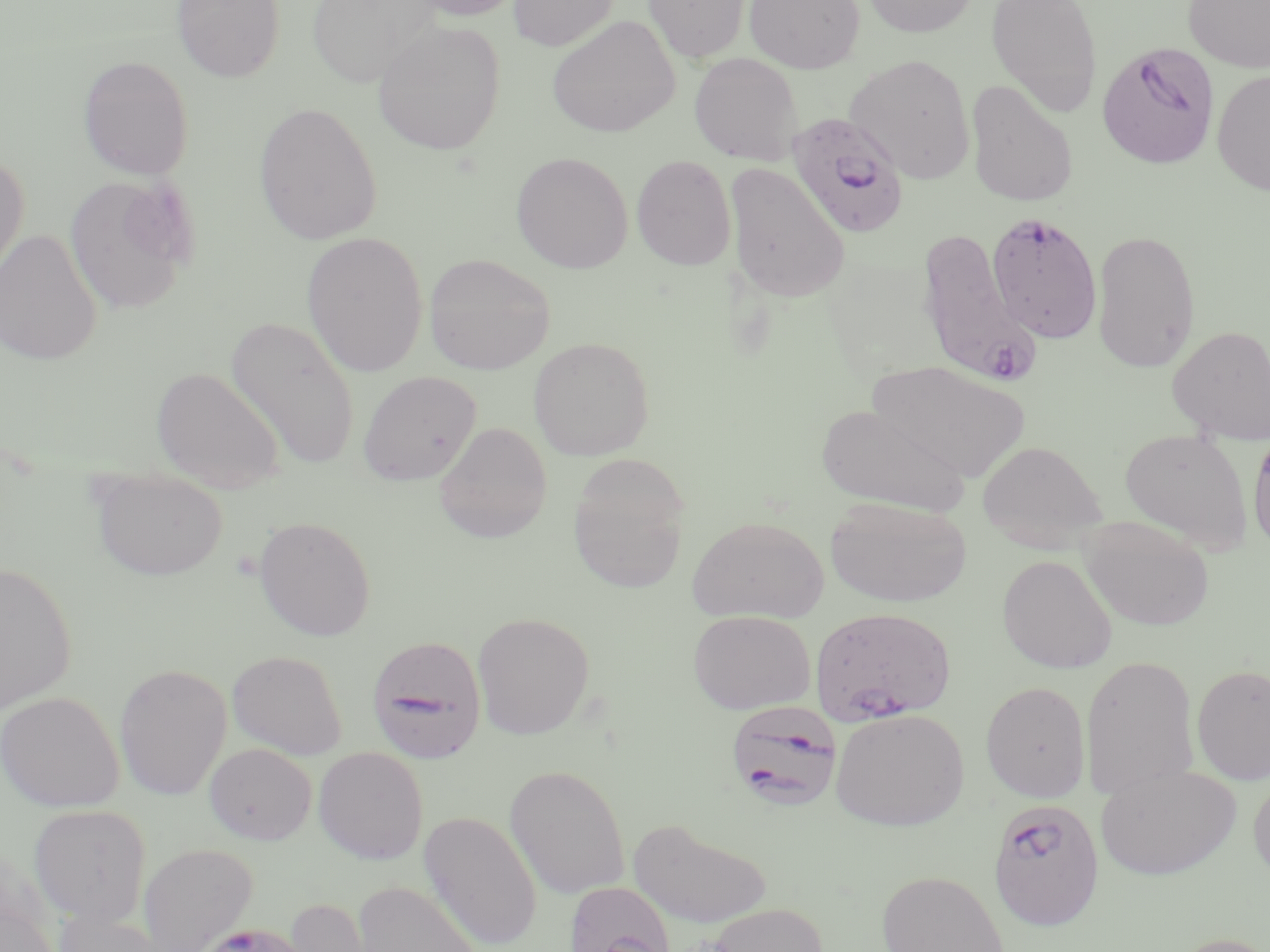

{
  "slide_level_diagnosis": "Plasmodium falciparum",
  "magnification": "1000x",
  "stain": "May-Grünwald-Giemsa",
  "plasmodium_falciparum_infected_red_blood_cell_locations": "approximate bounding boxes as named x1/y1/x2/y2 corners in pixels: (x1=1096, y1=42, x2=1220, y2=170), (x1=786, y1=112, x2=910, y2=239), (x1=985, y1=211, x2=1103, y2=343), (x1=915, y1=228, x2=1039, y2=385), (x1=810, y1=606, x2=957, y2=725), (x1=367, y1=635, x2=487, y2=763), (x1=728, y1=697, x2=846, y2=811), (x1=987, y1=797, x2=1105, y2=931)",
  "modality": "light microscopy",
  "preparation": "thin blood smear",
  "field_of_view": "single",
  "uninfected_red_blood_cell_locations": "approximate bounding boxes as named x1/y1/x2/y2 corners in pixels: (x1=171, y1=0, x2=285, y2=83), (x1=307, y1=0, x2=441, y2=87), (x1=405, y1=0, x2=527, y2=22), (x1=508, y1=0, x2=620, y2=51), (x1=643, y1=0, x2=750, y2=63), (x1=745, y1=0, x2=865, y2=73), (x1=861, y1=0, x2=980, y2=37), (x1=986, y1=0, x2=1103, y2=117), (x1=1183, y1=0, x2=1270, y2=73), (x1=547, y1=15, x2=680, y2=138), (x1=373, y1=21, x2=506, y2=155), (x1=689, y1=52, x2=802, y2=165), (x1=77, y1=54, x2=194, y2=181), (x1=846, y1=54, x2=976, y2=183), (x1=1212, y1=69, x2=1270, y2=196), (x1=965, y1=79, x2=1079, y2=207), (x1=254, y1=102, x2=382, y2=245), (x1=511, y1=151, x2=633, y2=273), (x1=0, y1=153, x2=30, y2=281), (x1=631, y1=154, x2=737, y2=271), (x1=724, y1=162, x2=849, y2=303), (x1=64, y1=176, x2=191, y2=315), (x1=0, y1=228, x2=102, y2=366), (x1=1091, y1=229, x2=1201, y2=372), (x1=302, y1=232, x2=428, y2=378), (x1=423, y1=252, x2=555, y2=375), (x1=226, y1=314, x2=361, y2=471), (x1=1168, y1=325, x2=1270, y2=444), (x1=528, y1=336, x2=655, y2=461), (x1=869, y1=360, x2=1030, y2=482), (x1=152, y1=367, x2=285, y2=493), (x1=357, y1=371, x2=481, y2=486), (x1=816, y1=402, x2=972, y2=516), (x1=434, y1=422, x2=552, y2=542), (x1=1247, y1=426, x2=1270, y2=558), (x1=1119, y1=427, x2=1254, y2=552), (x1=977, y1=439, x2=1107, y2=547), (x1=568, y1=458, x2=690, y2=594), (x1=89, y1=469, x2=229, y2=581), (x1=825, y1=497, x2=972, y2=608), (x1=687, y1=515, x2=829, y2=623), (x1=254, y1=516, x2=376, y2=641), (x1=1079, y1=518, x2=1215, y2=631), (x1=997, y1=554, x2=1118, y2=674), (x1=0, y1=561, x2=78, y2=714), (x1=687, y1=610, x2=815, y2=714), (x1=472, y1=611, x2=595, y2=739), (x1=227, y1=649, x2=348, y2=759), (x1=1081, y1=656, x2=1199, y2=801), (x1=114, y1=663, x2=232, y2=801), (x1=1191, y1=664, x2=1270, y2=785), (x1=980, y1=681, x2=1091, y2=803), (x1=1, y1=691, x2=124, y2=812), (x1=830, y1=708, x2=969, y2=831), (x1=204, y1=742, x2=317, y2=845), (x1=313, y1=746, x2=428, y2=865), (x1=1095, y1=763, x2=1241, y2=881), (x1=505, y1=764, x2=630, y2=899), (x1=1248, y1=769, x2=1270, y2=887), (x1=29, y1=804, x2=151, y2=926), (x1=418, y1=810, x2=542, y2=950), (x1=628, y1=817, x2=773, y2=928), (x1=138, y1=844, x2=259, y2=951), (x1=876, y1=869, x2=1010, y2=952), (x1=350, y1=880, x2=485, y2=952), (x1=564, y1=880, x2=677, y2=952), (x1=280, y1=896, x2=380, y2=952), (x1=0, y1=899, x2=58, y2=952), (x1=702, y1=902, x2=829, y2=952), (x1=51, y1=908, x2=168, y2=952), (x1=192, y1=920, x2=314, y2=952), (x1=1164, y1=931, x2=1270, y2=952)",
  "image_size": "1270×952 pixels"
}